Name the parasite shown.
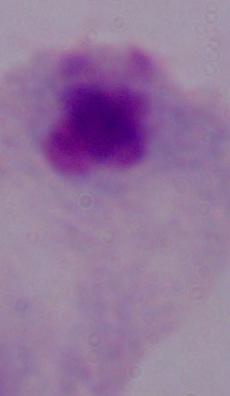
A trichomonad.

magnification = 1000x
modality = photomicrograph